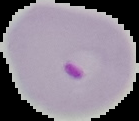

Summary:
  - Image size: 139×121 pixels
  - Preparation: thin blood smear
  - Result: Plasmodium parasites detected
  - Image type: segmented cell region on a black background